Report the malaria status of this cell.
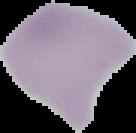
It is uninfected.

{
  "image_size": "136×133 pixels",
  "image_type": "segmented cell region with the area outside set to black",
  "preparation": "thin blood film"
}